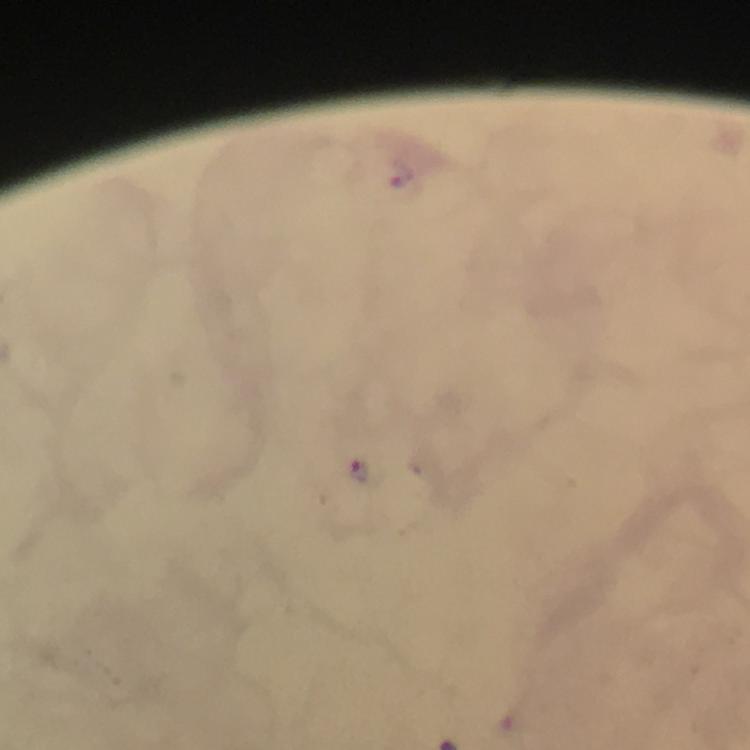

Approximate centers as {x, y} in pixels. Malaria parasite locations: {359, 470}. Image is 750×750 pixels. 100x magnification. Immersion oil applied. Photographed through the microscope with a smartphone camera. Thick smear. Giemsa stain. From a diagnostic examination for malaria. A crop from one field of view.